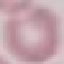
Summary:
  - Result: no malaria parasites detected
  - Capture: smartphone camera at the microscope eyepiece
  - Image type: cell patch, automatically extracted from a larger field of view and resized to 64 × 64 pixels
  - Stain: Giemsa
  - Preparation: thin blood smear